State the blood parasite species.
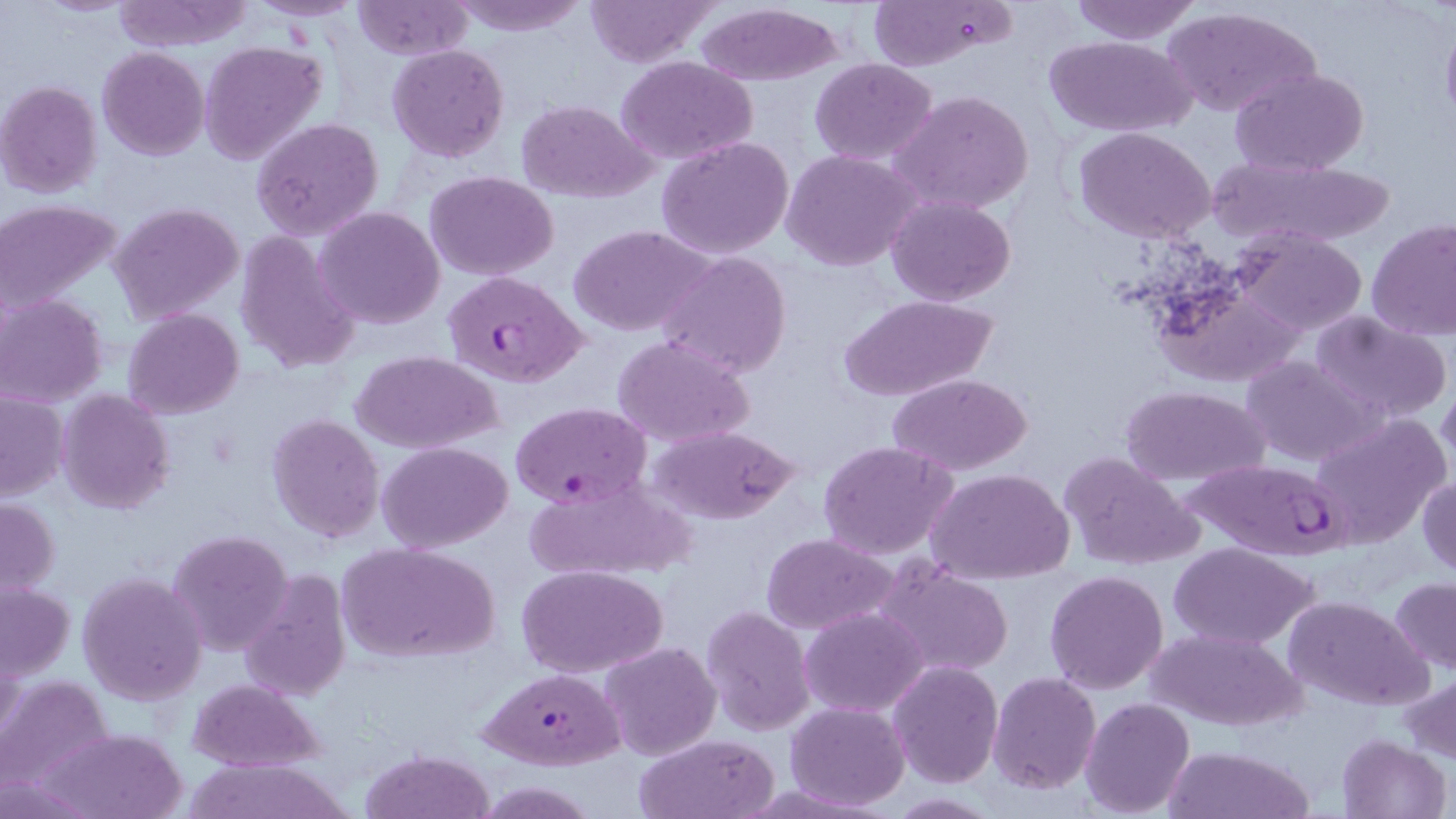
Plasmodium falciparum.

modality = optical microscopy
stain = May-Grünwald-Giemsa
field of view = single
image size = 1456×819 pixels
magnification = 1000x
preparation = thin blood film
Plasmodium falciparum-infected red blood cell locations = approximate bounding boxes as (x1, y1, x2, y2) in pixels: (442, 269, 589, 388), (510, 401, 652, 510), (1181, 459, 1350, 559), (479, 668, 624, 770)
uninfected red blood cell locations = approximate bounding boxes as (x1, y1, x2, y2) in pixels: (248, 0, 364, 22), (449, 0, 592, 36), (583, 0, 721, 67), (866, 0, 1015, 73), (1066, 0, 1204, 44), (111, 1, 254, 51), (352, 1, 472, 61), (693, 3, 849, 85), (1160, 4, 1321, 118), (1044, 34, 1195, 136), (199, 41, 328, 167), (386, 44, 510, 163), (97, 47, 209, 161), (616, 56, 757, 166), (809, 59, 938, 166), (1229, 67, 1372, 177), (1, 80, 103, 198), (888, 90, 1036, 216), (518, 99, 657, 202), (252, 117, 385, 240), (1075, 128, 1217, 244), (656, 135, 795, 260), (781, 149, 923, 271), (1204, 154, 1403, 254), (425, 170, 559, 280), (886, 195, 1016, 307), (3, 200, 121, 311), (109, 202, 245, 324), (316, 206, 444, 329), (1367, 216, 1456, 341), (570, 224, 714, 337), (1231, 229, 1368, 336), (235, 231, 361, 373), (656, 250, 793, 378), (1151, 279, 1310, 388), (841, 293, 997, 404), (0, 294, 107, 407), (1310, 308, 1453, 427), (124, 310, 243, 420), (611, 334, 755, 447), (353, 351, 501, 455), (1239, 356, 1381, 467), (889, 373, 1031, 475), (1438, 381, 1456, 470), (1119, 385, 1270, 488), (58, 389, 174, 514), (1, 391, 69, 502), (266, 412, 384, 543), (1310, 415, 1449, 550), (646, 424, 801, 525), (818, 440, 959, 560), (378, 441, 513, 551), (1058, 450, 1204, 572), (929, 468, 1073, 584), (1417, 474, 1456, 578), (517, 475, 698, 582), (0, 497, 61, 598), (167, 529, 295, 657), (760, 534, 898, 635), (339, 541, 498, 665), (1168, 541, 1320, 649), (872, 558, 1017, 678), (519, 565, 666, 678), (238, 570, 352, 702), (1044, 570, 1168, 694), (77, 571, 206, 705), (1390, 577, 1456, 674), (1, 583, 75, 681), (1285, 595, 1431, 710), (700, 606, 815, 734), (799, 607, 928, 716), (1147, 626, 1306, 731), (599, 641, 721, 762), (888, 660, 1003, 789), (1405, 669, 1456, 765), (989, 672, 1101, 794), (0, 678, 116, 801), (188, 679, 323, 772), (1081, 698, 1195, 817), (785, 703, 910, 811), (44, 726, 189, 819), (635, 733, 778, 818), (1336, 735, 1452, 819), (1162, 746, 1311, 819), (360, 748, 491, 818), (185, 756, 349, 819), (477, 779, 598, 818)